Identify the blood parasite species.
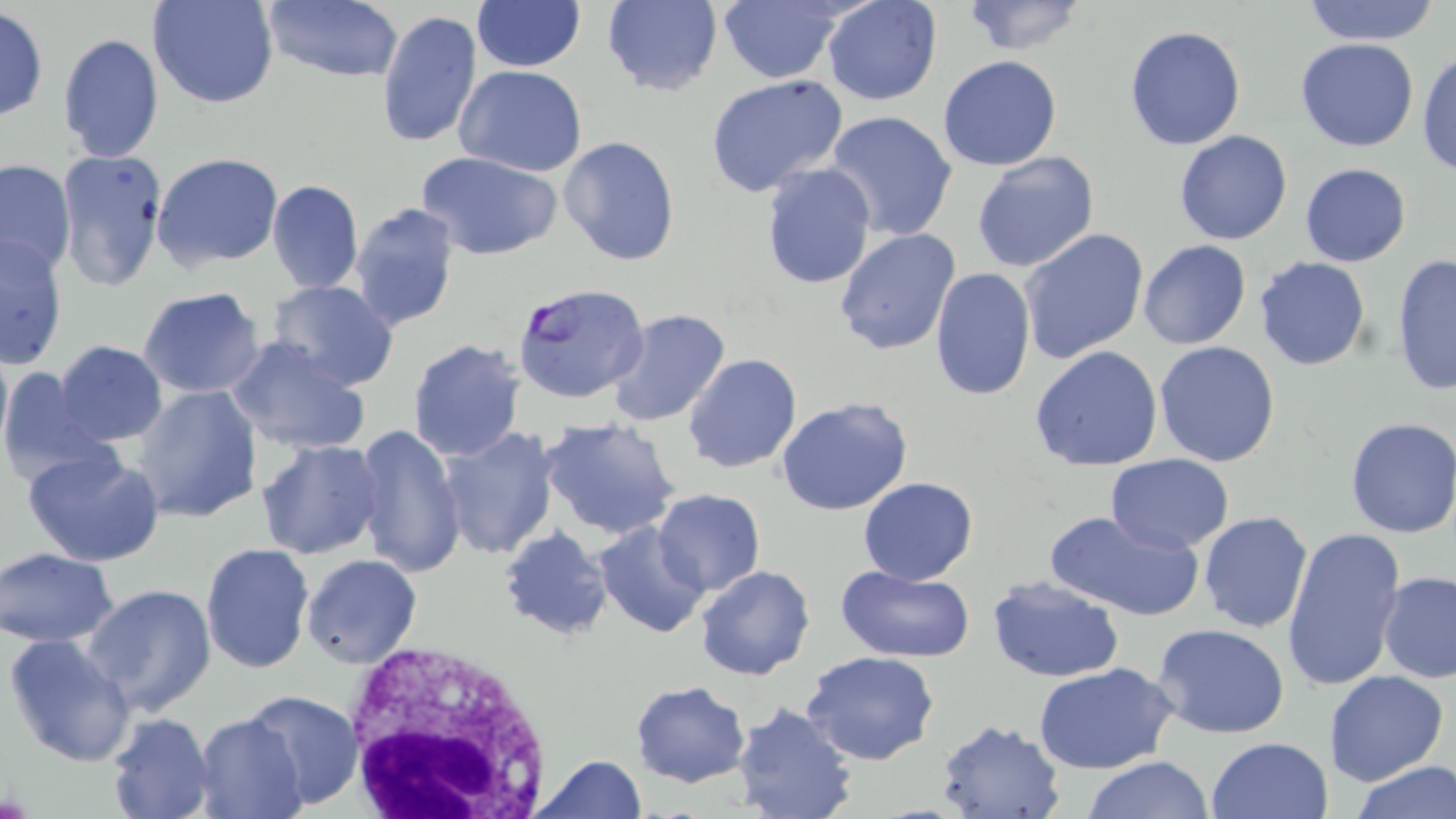

Plasmodium falciparum.

Approximate bounding boxes as (x1, y1, x2, y2) in pixels. White blood cell locations: (337, 639, 555, 817). Plasmodium falciparum-infected red blood cell locations: (515, 283, 657, 406). Uninfected red blood cell locations: (147, 0, 280, 110), (260, 0, 406, 84), (470, 0, 584, 71), (601, 0, 723, 96), (714, 0, 851, 85), (822, 0, 943, 106), (960, 1, 1090, 55), (1297, 2, 1444, 45), (0, 8, 48, 121), (374, 8, 482, 149), (1123, 23, 1248, 151), (56, 32, 165, 164), (1295, 38, 1420, 152), (1416, 47, 1456, 179), (937, 55, 1062, 172), (454, 65, 588, 178), (704, 74, 849, 197), (825, 110, 958, 243), (1174, 129, 1292, 245), (558, 135, 681, 268), (54, 148, 168, 292), (415, 150, 562, 262), (151, 152, 284, 271), (972, 152, 1100, 274), (0, 159, 76, 273), (1299, 162, 1412, 267), (759, 164, 877, 289), (266, 178, 363, 294), (349, 202, 462, 332), (834, 227, 961, 355), (1018, 227, 1149, 364), (0, 233, 70, 370), (1138, 239, 1251, 350), (1391, 251, 1456, 399), (1254, 257, 1371, 372), (927, 266, 1036, 402), (266, 279, 401, 392), (137, 287, 266, 398), (605, 309, 732, 428), (0, 338, 12, 461), (227, 338, 370, 455), (407, 339, 525, 461), (56, 340, 167, 445), (1153, 340, 1282, 467), (1029, 345, 1163, 472), (681, 353, 803, 474), (0, 367, 112, 488), (133, 384, 263, 523), (775, 396, 913, 515), (539, 418, 681, 540), (1343, 418, 1456, 539), (354, 423, 467, 578), (437, 428, 560, 559), (257, 439, 384, 558), (23, 447, 166, 569), (1106, 455, 1235, 553), (857, 477, 979, 585), (653, 490, 766, 596), (1042, 508, 1204, 620), (1198, 510, 1313, 634), (593, 520, 710, 639), (1281, 524, 1409, 694), (498, 526, 614, 642), (199, 542, 315, 673), (0, 547, 121, 648), (301, 554, 423, 668), (696, 564, 815, 681), (835, 564, 976, 662), (1377, 573, 1456, 685), (987, 575, 1125, 683), (84, 584, 216, 717), (1153, 622, 1292, 740), (3, 631, 137, 768), (801, 650, 940, 766), (1033, 662, 1177, 774), (1325, 669, 1449, 788), (629, 681, 751, 786), (243, 686, 364, 810), (729, 702, 859, 819), (104, 712, 213, 819), (193, 713, 308, 819), (937, 719, 1065, 818), (1205, 736, 1333, 819), (530, 754, 648, 819), (1082, 756, 1215, 819), (1350, 760, 1455, 818). May-Grünwald-Giemsa stain. Optical microscopy. One field of a larger specimen. Thin blood smear. Captured at 1000x magnification. Image is 1456×819 pixels.